Comment on the morphology of the red blood cells.
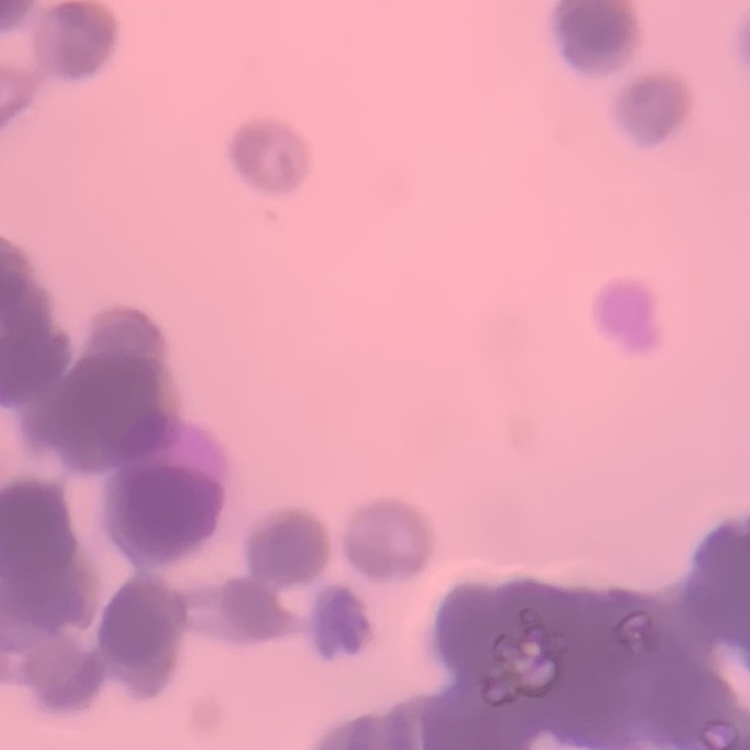

Rouleaux formation.

Summary:
  - Preparation: thin blood film
  - Stain: Field's or Giemsa
  - Image type: one tile cut from a larger photomicrograph